State which parasite is depicted.
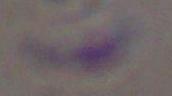
Toxoplasma gondii.

Summary:
  - Magnification: 1000x
  - Modality: micrograph